Identify the parasite.
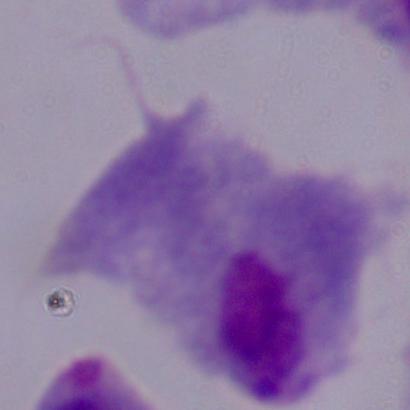
A trichomonad.

magnification = 1000x
modality = photomicrograph